Locate every uninfected red blood cell.
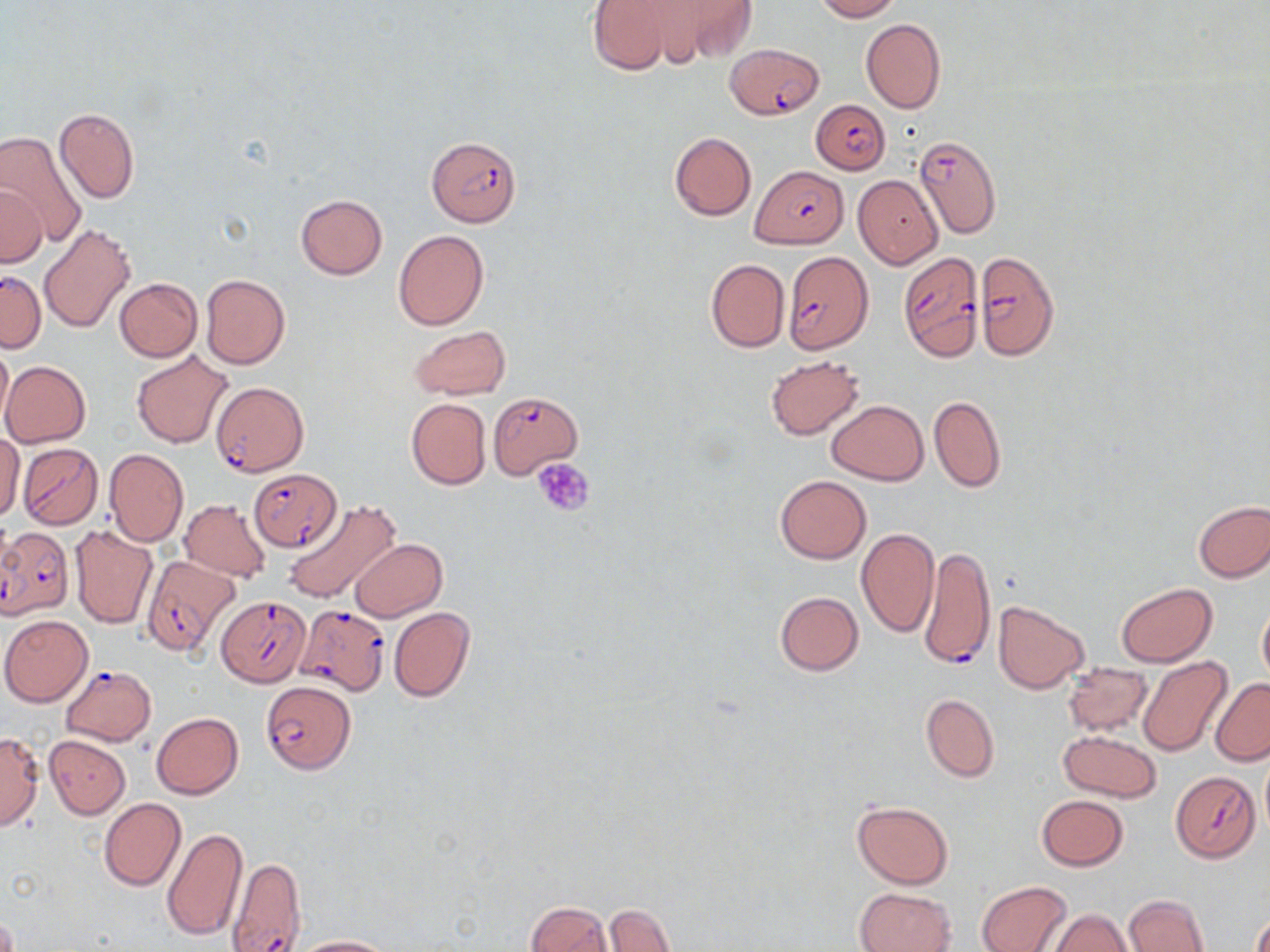

Approximate bounding boxes as named x1/y1/x2/y2 corners in pixels.
Uninfected red blood cells: (x1=585, y1=0, x2=678, y2=75), (x1=633, y1=0, x2=756, y2=66), (x1=815, y1=0, x2=899, y2=21), (x1=861, y1=19, x2=946, y2=112), (x1=54, y1=108, x2=140, y2=204), (x1=1, y1=132, x2=89, y2=249), (x1=669, y1=132, x2=756, y2=220), (x1=853, y1=175, x2=943, y2=269), (x1=0, y1=184, x2=44, y2=267), (x1=294, y1=194, x2=388, y2=279), (x1=39, y1=225, x2=136, y2=335), (x1=392, y1=230, x2=488, y2=331), (x1=705, y1=258, x2=789, y2=353), (x1=201, y1=274, x2=290, y2=369), (x1=115, y1=279, x2=203, y2=360), (x1=411, y1=326, x2=511, y2=400), (x1=0, y1=339, x2=13, y2=428), (x1=132, y1=351, x2=235, y2=449), (x1=765, y1=355, x2=865, y2=439), (x1=1, y1=360, x2=91, y2=447), (x1=929, y1=395, x2=1006, y2=492), (x1=406, y1=398, x2=491, y2=489), (x1=828, y1=400, x2=928, y2=484), (x1=1, y1=432, x2=24, y2=521), (x1=104, y1=448, x2=188, y2=546), (x1=774, y1=475, x2=871, y2=564), (x1=180, y1=499, x2=272, y2=583), (x1=284, y1=499, x2=401, y2=605), (x1=1193, y1=501, x2=1270, y2=581), (x1=69, y1=524, x2=157, y2=628), (x1=855, y1=528, x2=939, y2=637), (x1=350, y1=538, x2=448, y2=622), (x1=1116, y1=583, x2=1216, y2=667), (x1=775, y1=591, x2=864, y2=675), (x1=993, y1=601, x2=1088, y2=693), (x1=1256, y1=601, x2=1270, y2=688), (x1=388, y1=607, x2=475, y2=702), (x1=1, y1=615, x2=93, y2=706), (x1=1136, y1=657, x2=1232, y2=757), (x1=1063, y1=662, x2=1152, y2=736), (x1=1210, y1=678, x2=1270, y2=765), (x1=921, y1=693, x2=999, y2=782), (x1=152, y1=712, x2=243, y2=799), (x1=1059, y1=731, x2=1162, y2=801), (x1=0, y1=732, x2=44, y2=831), (x1=44, y1=735, x2=129, y2=818), (x1=1259, y1=751, x2=1270, y2=836), (x1=1037, y1=795, x2=1129, y2=871), (x1=99, y1=798, x2=186, y2=891), (x1=851, y1=800, x2=953, y2=890), (x1=162, y1=827, x2=248, y2=941), (x1=977, y1=881, x2=1070, y2=952), (x1=855, y1=887, x2=956, y2=952), (x1=1121, y1=893, x2=1211, y2=952), (x1=526, y1=901, x2=613, y2=952), (x1=603, y1=903, x2=674, y2=952), (x1=1048, y1=909, x2=1132, y2=952), (x1=1250, y1=911, x2=1270, y2=952), (x1=287, y1=935, x2=397, y2=952).

Plasmodium falciparum-infected red blood cell locations: (x1=725, y1=43, x2=824, y2=120), (x1=810, y1=100, x2=889, y2=173), (x1=914, y1=133, x2=1003, y2=238), (x1=426, y1=137, x2=521, y2=226), (x1=750, y1=165, x2=848, y2=248), (x1=783, y1=251, x2=873, y2=354), (x1=896, y1=252, x2=985, y2=360), (x1=976, y1=252, x2=1060, y2=361), (x1=0, y1=274, x2=47, y2=355), (x1=210, y1=380, x2=310, y2=482), (x1=488, y1=391, x2=581, y2=478), (x1=18, y1=442, x2=103, y2=529), (x1=249, y1=467, x2=342, y2=552), (x1=0, y1=526, x2=75, y2=619), (x1=922, y1=545, x2=995, y2=670), (x1=141, y1=555, x2=241, y2=658), (x1=217, y1=595, x2=307, y2=692), (x1=294, y1=603, x2=391, y2=695), (x1=59, y1=664, x2=156, y2=745), (x1=261, y1=682, x2=356, y2=774), (x1=1170, y1=771, x2=1260, y2=863), (x1=227, y1=856, x2=307, y2=952). Platelet locations: (x1=535, y1=458, x2=596, y2=515). Slide-level diagnosis: Plasmodium falciparum. Image is 1270×952 pixels. One field of a larger specimen. May-Grünwald-Giemsa stain. 1000x magnification. Thin blood film. Optical microscopy.